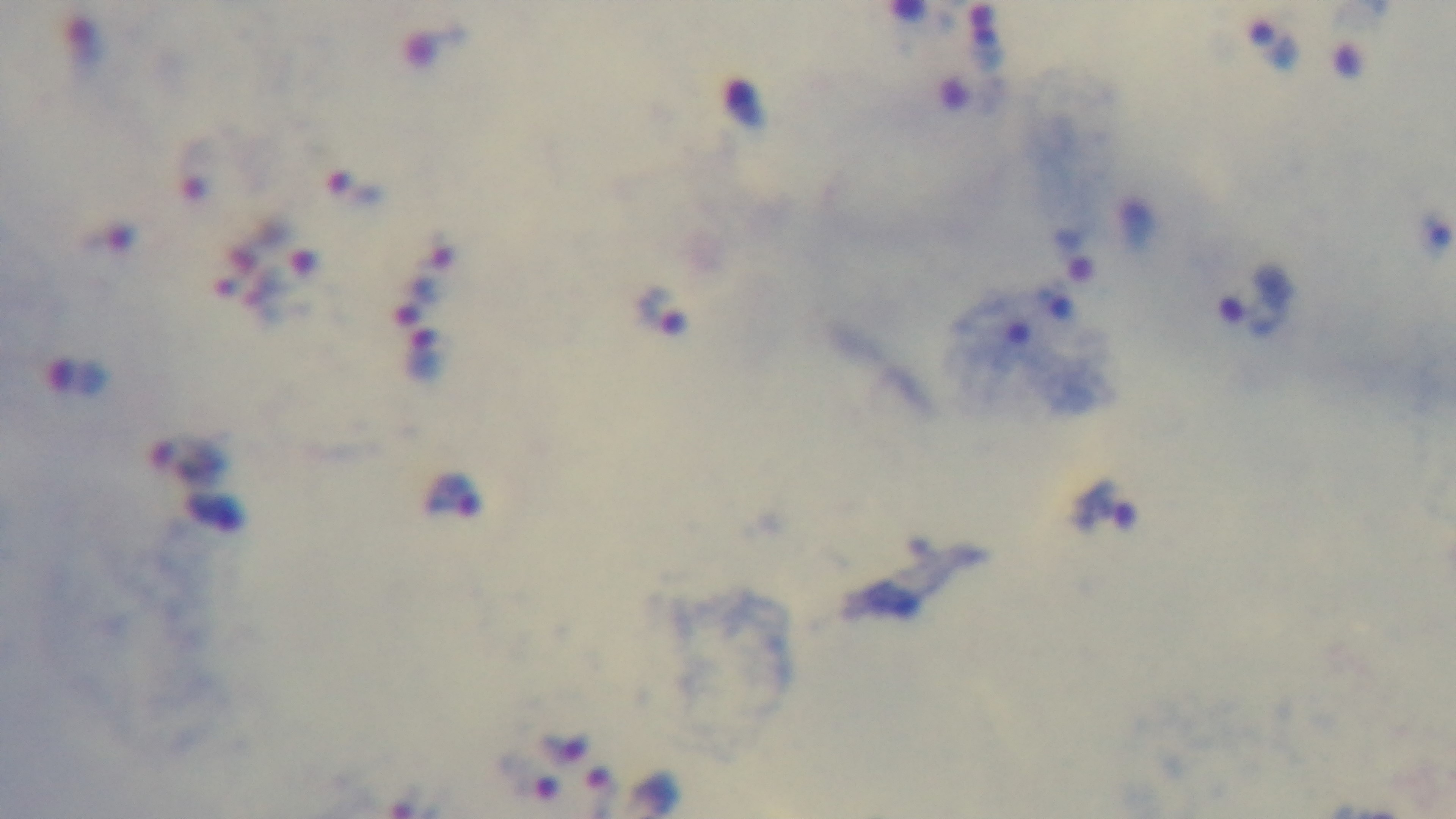 Photomicrograph. Oil-immersion objective, 100x. One field from the slide. Captured with a mounted 4K digital camera. Giemsa stain. Preparation: thick smear. Malaria status: infected.